Locate every leukocyte (white blood cell).
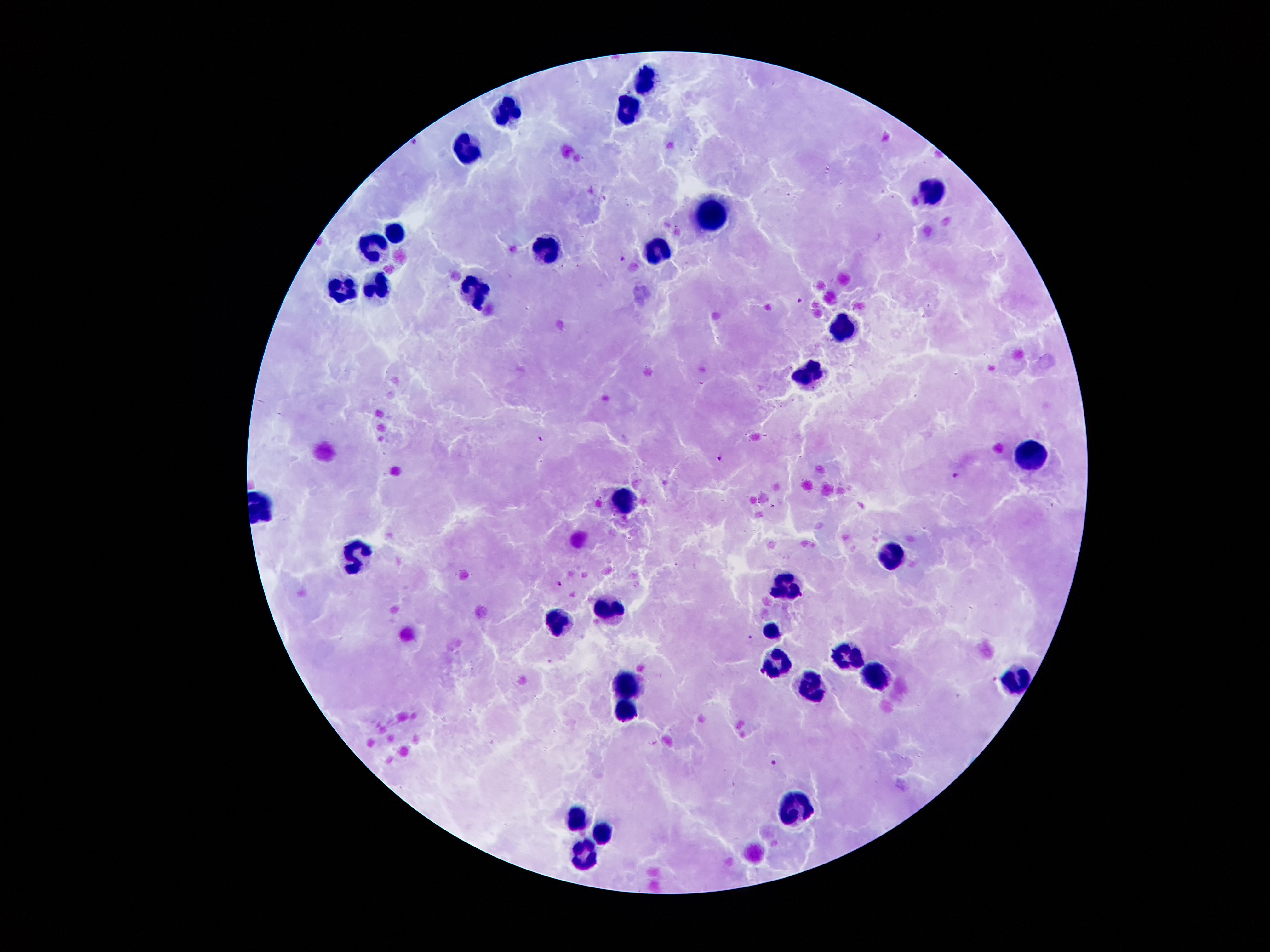

Approximate centers as (x, y) in pixels.
Leukocytes: (646, 77), (509, 110), (625, 110), (467, 146), (933, 187), (712, 214), (395, 232), (372, 247), (543, 249), (655, 249), (377, 283), (341, 287), (474, 291), (842, 327), (811, 371), (1026, 452), (622, 496), (893, 554), (356, 558), (784, 585), (609, 609), (558, 619), (771, 625), (849, 653), (777, 660), (875, 672), (1015, 681), (806, 683), (631, 688), (628, 707), (798, 806), (578, 811), (603, 828), (584, 851).

{
  "stain": "Giemsa",
  "field_of_view": "single",
  "malaria_parasite_locations": "approximate centers as (x, y) in pixels: (414, 141), (624, 260), (800, 302), (540, 438), (718, 458), (954, 476), (559, 583), (750, 636), (775, 762)",
  "patient_malaria_status": "infected with Plasmodium falciparum",
  "capture": "smartphone camera through the microscope eyepiece",
  "image_size": "1270×952 pixels",
  "magnification": "100x",
  "preparation": "thick blood film"
}